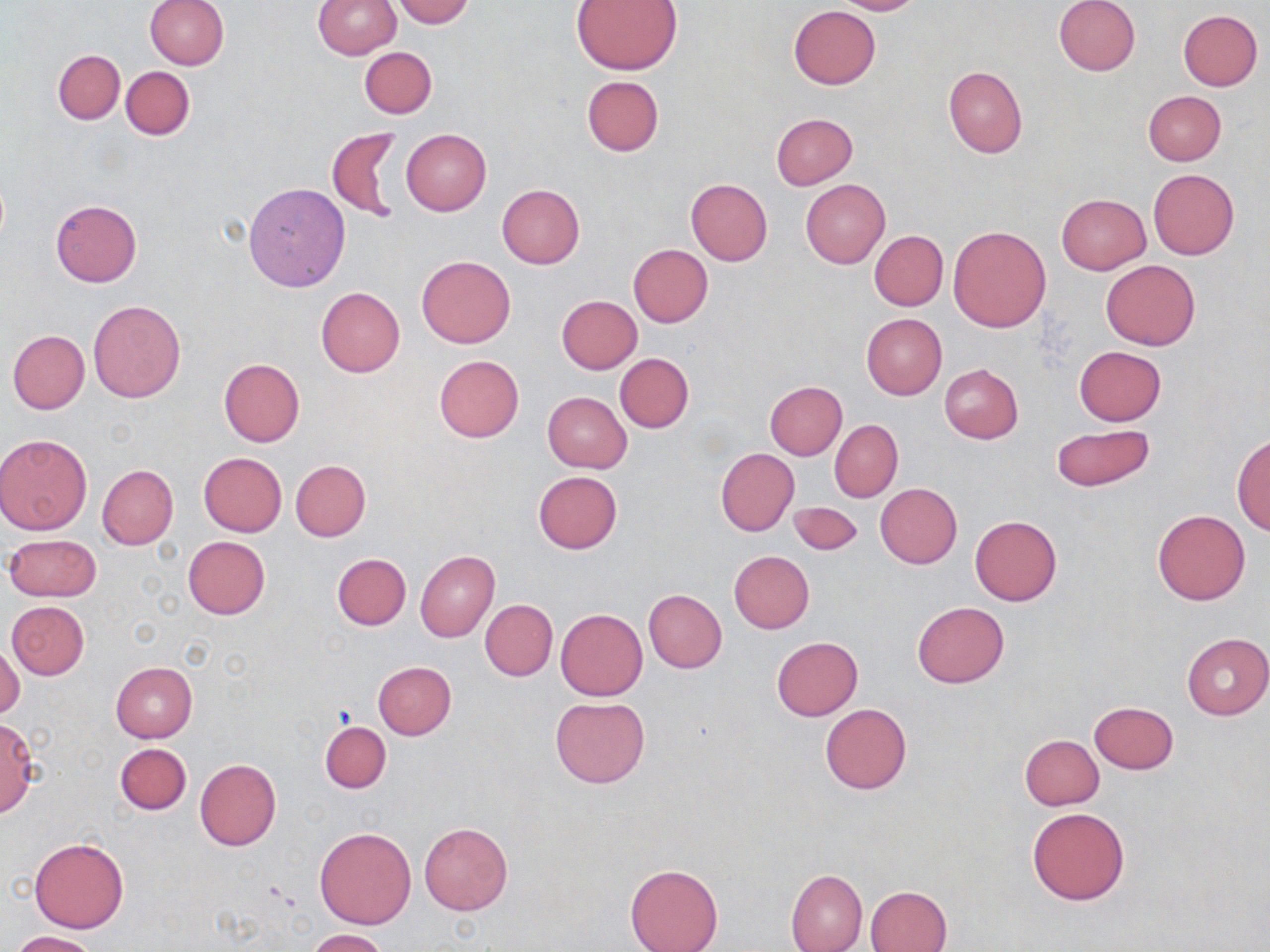
Approximate bounding boxes as named x1/y1/x2/y2 corners in pixels. Uninfected red blood cell locations: (x1=145, y1=0, x2=228, y2=70), (x1=313, y1=0, x2=400, y2=59), (x1=392, y1=0, x2=474, y2=27), (x1=832, y1=0, x2=925, y2=15), (x1=1054, y1=0, x2=1141, y2=76), (x1=572, y1=1, x2=683, y2=74), (x1=788, y1=5, x2=880, y2=89), (x1=1178, y1=9, x2=1263, y2=90), (x1=359, y1=46, x2=437, y2=120), (x1=52, y1=49, x2=125, y2=124), (x1=121, y1=66, x2=194, y2=140), (x1=943, y1=66, x2=1026, y2=157), (x1=582, y1=75, x2=664, y2=156), (x1=1143, y1=90, x2=1226, y2=165), (x1=770, y1=113, x2=857, y2=190), (x1=326, y1=128, x2=403, y2=224), (x1=402, y1=129, x2=492, y2=214), (x1=1147, y1=169, x2=1240, y2=260), (x1=686, y1=179, x2=773, y2=265), (x1=801, y1=179, x2=889, y2=268), (x1=243, y1=183, x2=350, y2=291), (x1=498, y1=184, x2=584, y2=269), (x1=1056, y1=193, x2=1151, y2=274), (x1=51, y1=200, x2=142, y2=287), (x1=947, y1=225, x2=1052, y2=333), (x1=870, y1=230, x2=948, y2=310), (x1=629, y1=244, x2=712, y2=327), (x1=416, y1=256, x2=515, y2=349), (x1=1100, y1=260, x2=1200, y2=350), (x1=316, y1=288, x2=405, y2=378), (x1=557, y1=295, x2=641, y2=373), (x1=88, y1=300, x2=186, y2=403), (x1=862, y1=314, x2=946, y2=400), (x1=8, y1=330, x2=89, y2=414), (x1=1074, y1=346, x2=1166, y2=425), (x1=615, y1=353, x2=694, y2=432), (x1=433, y1=355, x2=524, y2=442), (x1=219, y1=358, x2=305, y2=446), (x1=939, y1=364, x2=1023, y2=444), (x1=765, y1=381, x2=846, y2=460), (x1=543, y1=392, x2=632, y2=473), (x1=830, y1=419, x2=903, y2=502), (x1=1050, y1=424, x2=1155, y2=492), (x1=0, y1=432, x2=94, y2=535), (x1=1232, y1=433, x2=1269, y2=534), (x1=716, y1=448, x2=799, y2=537), (x1=198, y1=452, x2=286, y2=536), (x1=290, y1=460, x2=370, y2=541), (x1=97, y1=465, x2=178, y2=549), (x1=532, y1=470, x2=622, y2=554), (x1=875, y1=483, x2=962, y2=568), (x1=789, y1=501, x2=863, y2=556), (x1=1153, y1=509, x2=1250, y2=605), (x1=970, y1=516, x2=1061, y2=606), (x1=5, y1=534, x2=101, y2=601), (x1=182, y1=536, x2=270, y2=618), (x1=415, y1=551, x2=499, y2=642), (x1=730, y1=551, x2=814, y2=633), (x1=332, y1=553, x2=410, y2=630), (x1=644, y1=590, x2=727, y2=673), (x1=480, y1=599, x2=557, y2=681), (x1=6, y1=600, x2=89, y2=679), (x1=912, y1=601, x2=1009, y2=687), (x1=555, y1=609, x2=647, y2=700), (x1=1181, y1=633, x2=1269, y2=720), (x1=772, y1=637, x2=863, y2=720), (x1=1, y1=639, x2=23, y2=720), (x1=374, y1=661, x2=456, y2=739), (x1=110, y1=662, x2=197, y2=742), (x1=549, y1=696, x2=651, y2=788), (x1=1089, y1=701, x2=1178, y2=774), (x1=820, y1=704, x2=912, y2=793), (x1=0, y1=718, x2=38, y2=817), (x1=319, y1=721, x2=390, y2=793), (x1=1019, y1=735, x2=1103, y2=810), (x1=115, y1=743, x2=190, y2=814), (x1=195, y1=759, x2=282, y2=851), (x1=1027, y1=808, x2=1129, y2=904), (x1=419, y1=822, x2=512, y2=915), (x1=314, y1=826, x2=417, y2=929), (x1=29, y1=838, x2=129, y2=932), (x1=625, y1=863, x2=723, y2=952), (x1=786, y1=869, x2=867, y2=952), (x1=865, y1=885, x2=950, y2=952), (x1=305, y1=929, x2=388, y2=951), (x1=10, y1=930, x2=100, y2=952). Slide-level diagnosis: no evidence of blood parasites. Optical microscopy. Image is 1270×952 pixels. Thin blood smear. One field of a larger specimen. 1000x magnification. May-Grünwald-Giemsa-stained preparation.